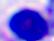 Photomicrograph. 400x magnification. A white blood cell is shown.